Locate every blood parasite and identify its species.
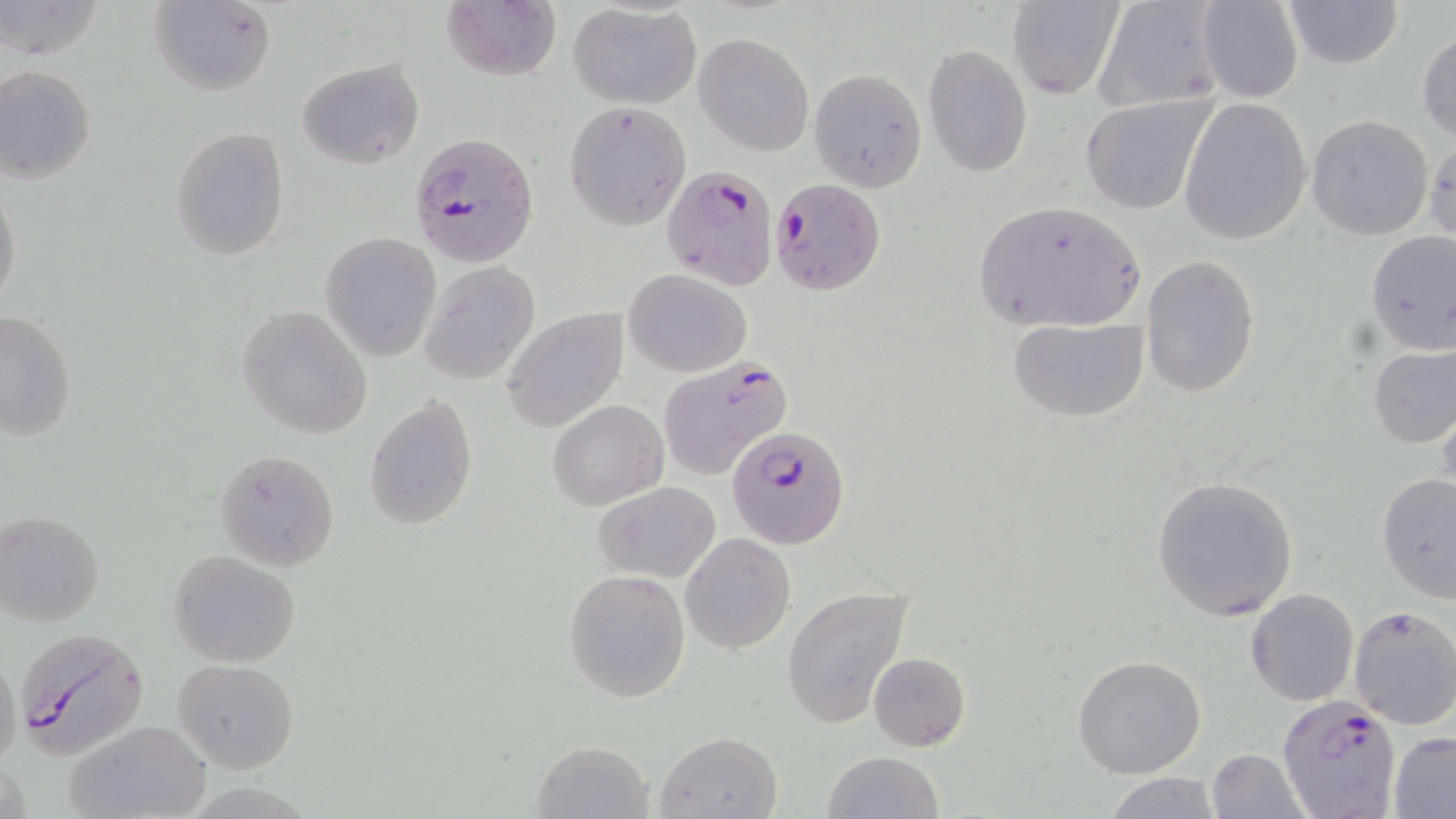
Approximate bounding boxes as (x1,y1)-(x2,y2) corner pairs in pixels.
Plasmodium falciparum-infected red blood cells: (409,131)-(539,267), (662,165)-(780,291), (769,178)-(887,298), (657,357)-(794,480), (729,427)-(851,548), (14,629)-(151,761), (1277,696)-(1402,819).
No Plasmodium ovale, Plasmodium malariae, Plasmodium vivax, Babesia divergens, or Trypanosoma brucei observed.

{
  "slide_level_diagnosis": "Plasmodium falciparum",
  "stain": "May-Grünwald-Giemsa",
  "uninfected_red_blood_cell_locations": "approximate bounding boxes as (x1,y1)-(x2,y2) corner pairs in pixels: (149,0)-(276,97), (1006,0)-(1124,100), (1092,0)-(1227,113), (1194,0)-(1305,104), (1280,0)-(1404,70), (0,1)-(106,61), (442,1)-(561,82), (570,2)-(701,109), (1417,30)-(1456,146), (694,32)-(813,155), (922,43)-(1032,177), (296,58)-(423,169), (0,64)-(97,185), (808,67)-(927,190), (1081,93)-(1214,215), (1177,97)-(1313,245), (563,101)-(692,230), (1305,114)-(1434,240), (170,126)-(290,260), (0,184)-(22,310), (972,200)-(1148,334), (1363,231)-(1456,355), (320,232)-(441,362), (1141,253)-(1259,400), (419,259)-(543,385), (621,269)-(751,378), (236,305)-(371,439), (501,308)-(629,433), (0,311)-(76,441), (1009,317)-(1147,421), (1367,344)-(1455,449), (1436,388)-(1456,507), (364,395)-(476,530), (547,399)-(668,509), (215,450)-(337,571), (1376,472)-(1456,603), (1150,474)-(1299,622), (593,479)-(721,585), (0,510)-(105,627), (680,532)-(796,655), (169,550)-(301,668), (564,569)-(690,702), (781,585)-(914,730), (1246,587)-(1360,707), (1349,605)-(1456,730), (0,646)-(21,779), (867,652)-(970,751), (1072,653)-(1206,777), (173,657)-(298,774), (63,719)-(213,819), (655,730)-(782,818), (1388,731)-(1456,816), (531,740)-(653,818), (1208,747)-(1307,817), (822,750)-(944,819), (1105,771)-(1221,819)",
  "modality": "optical microscopy",
  "magnification": "1000x",
  "field_of_view": "single",
  "image_size": "1456×819 pixels",
  "preparation": "thin blood smear"
}